Point out each leukocyte.
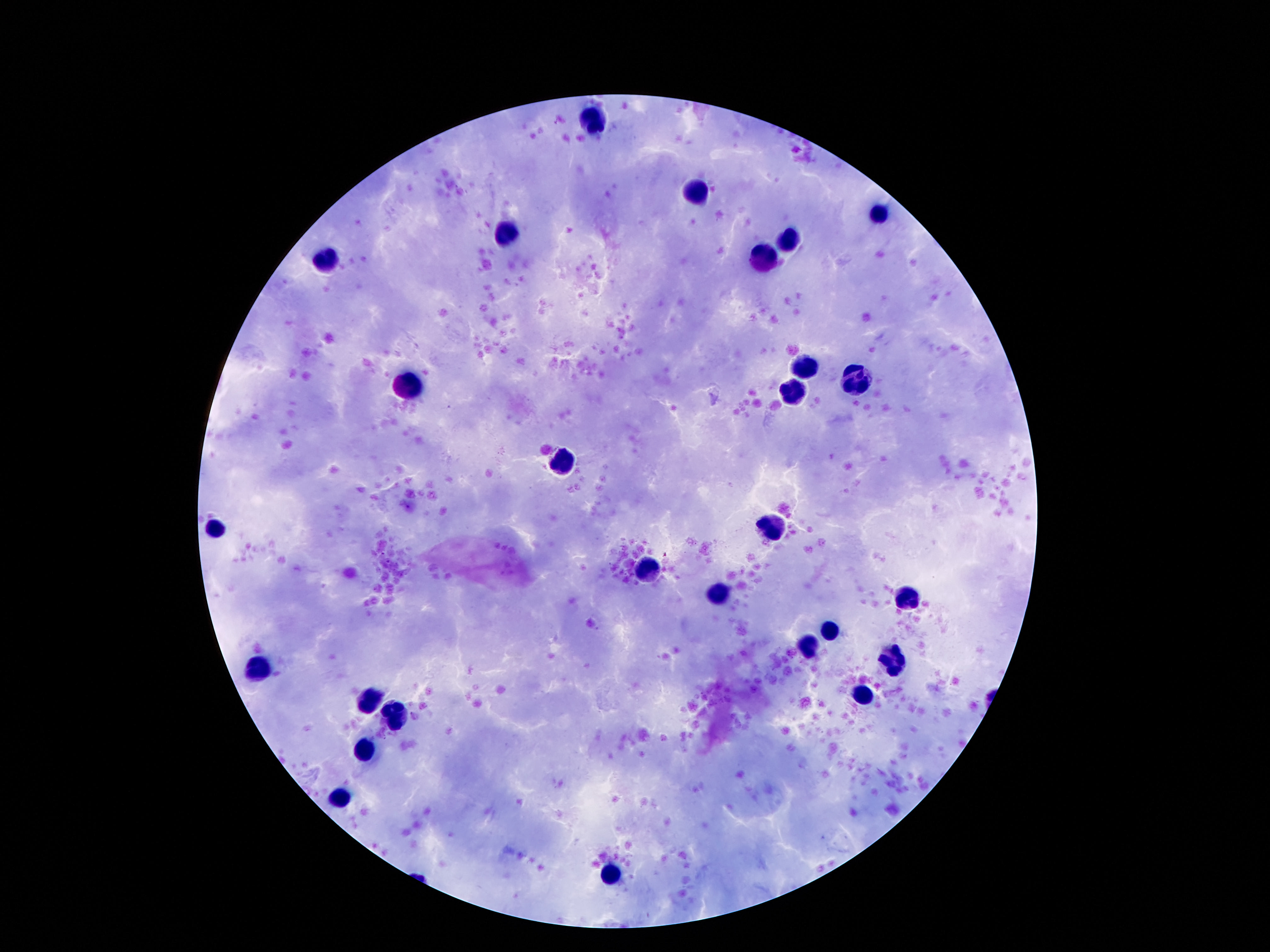

Approximate object centers, in pixels from the top-left corner.
Leukocytes: (x=592, y=119), (x=695, y=194), (x=881, y=215), (x=506, y=235), (x=790, y=235), (x=323, y=255), (x=762, y=261), (x=805, y=365), (x=857, y=379), (x=409, y=383), (x=786, y=391), (x=562, y=459), (x=217, y=526), (x=773, y=526), (x=652, y=571), (x=719, y=594), (x=909, y=597), (x=829, y=630), (x=807, y=645), (x=891, y=658), (x=258, y=668), (x=861, y=694), (x=370, y=696), (x=396, y=717), (x=366, y=748), (x=342, y=797), (x=611, y=871).

Single field of view. Giemsa-stained preparation. Thick blood film. 100x magnification. Image is 1270×952 pixels. Photographed through the microscope eyepiece with a smartphone camera. Patient malaria status: not infected.